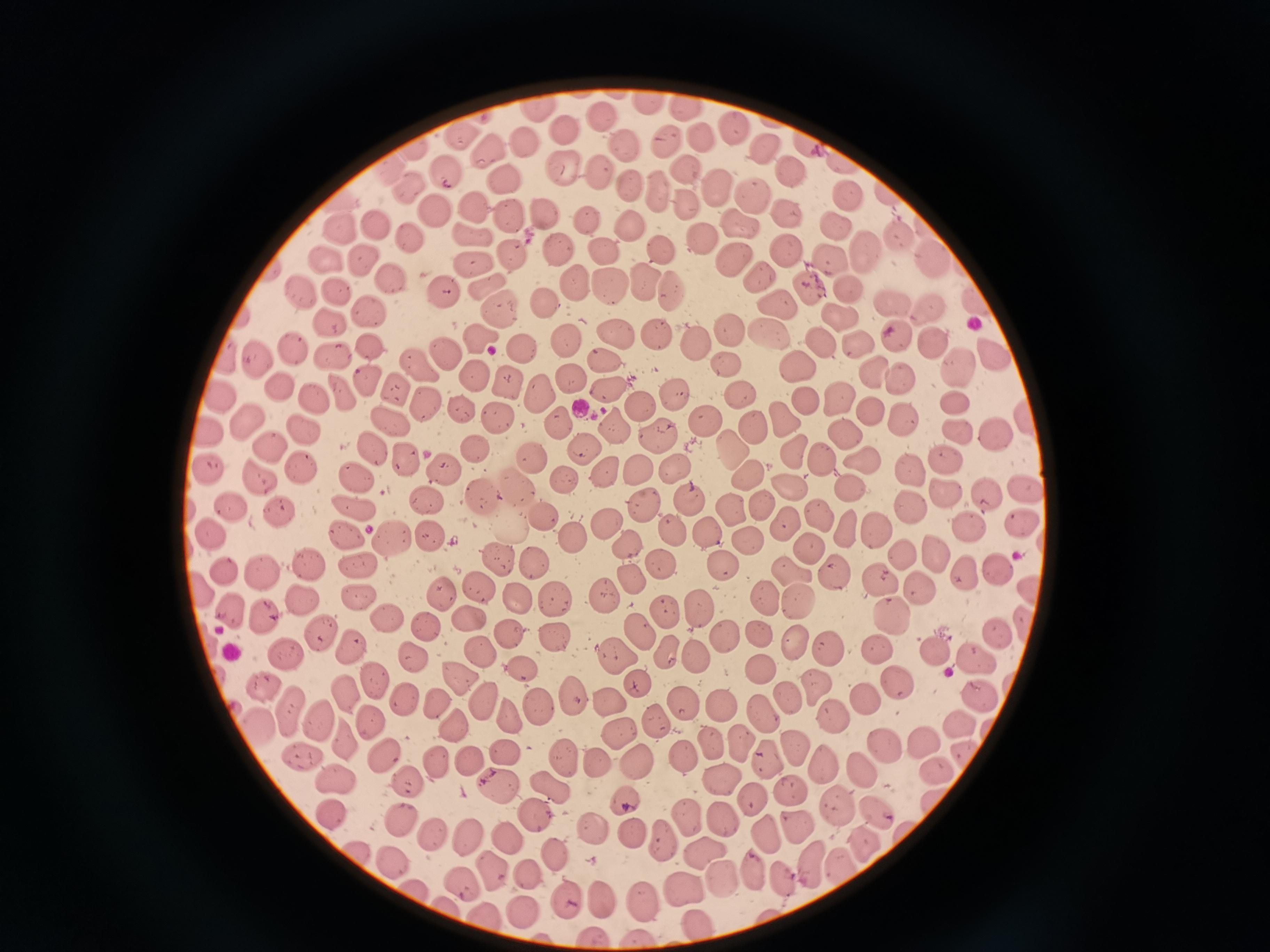
Approximate object centers, in pixels from the top-left corner.
Summary:
  - Cell locations: (x=648, y=104), (x=687, y=108), (x=541, y=109), (x=601, y=117), (x=735, y=128), (x=566, y=134), (x=465, y=137), (x=528, y=141), (x=665, y=141), (x=703, y=142), (x=811, y=144), (x=764, y=146), (x=414, y=148), (x=625, y=148), (x=490, y=154), (x=849, y=159), (x=391, y=170), (x=563, y=171), (x=597, y=171), (x=686, y=171), (x=450, y=172), (x=792, y=172), (x=504, y=181), (x=632, y=185), (x=716, y=186), (x=655, y=188), (x=409, y=193), (x=851, y=197), (x=344, y=198), (x=752, y=198), (x=685, y=202), (x=475, y=208), (x=544, y=211), (x=432, y=213), (x=788, y=215), (x=513, y=217), (x=584, y=219), (x=738, y=224), (x=629, y=226), (x=841, y=226), (x=378, y=227), (x=347, y=229), (x=467, y=232), (x=898, y=234), (x=409, y=237), (x=703, y=238), (x=663, y=248), (x=785, y=248), (x=512, y=249), (x=559, y=251), (x=605, y=252), (x=870, y=255), (x=731, y=256), (x=328, y=258), (x=472, y=261), (x=833, y=261), (x=364, y=262), (x=935, y=262), (x=270, y=267), (x=760, y=275), (x=644, y=278), (x=392, y=280), (x=574, y=285), (x=485, y=287), (x=605, y=287), (x=808, y=288), (x=444, y=290), (x=850, y=290), (x=667, y=291), (x=338, y=292), (x=305, y=293), (x=776, y=299), (x=982, y=302), (x=544, y=303), (x=892, y=303), (x=502, y=307), (x=931, y=308), (x=370, y=314), (x=839, y=316), (x=332, y=321), (x=731, y=329), (x=654, y=332), (x=616, y=333), (x=769, y=333), (x=897, y=333), (x=480, y=338), (x=565, y=339), (x=934, y=343), (x=519, y=344), (x=822, y=344), (x=859, y=344), (x=697, y=345), (x=368, y=346), (x=295, y=350), (x=446, y=354), (x=605, y=355), (x=998, y=355), (x=225, y=356), (x=332, y=357), (x=257, y=360), (x=726, y=363), (x=794, y=363), (x=420, y=365), (x=961, y=365), (x=874, y=374), (x=476, y=375), (x=571, y=377), (x=368, y=379), (x=903, y=380), (x=506, y=382), (x=279, y=385), (x=400, y=388), (x=537, y=392), (x=606, y=392), (x=340, y=394), (x=678, y=394), (x=740, y=394), (x=220, y=396), (x=310, y=397), (x=429, y=400), (x=843, y=400), (x=806, y=401), (x=954, y=401), (x=463, y=408), (x=644, y=409), (x=871, y=415), (x=905, y=416), (x=499, y=417), (x=784, y=418), (x=247, y=419), (x=1029, y=419), (x=557, y=420), (x=705, y=420), (x=394, y=421), (x=613, y=428), (x=754, y=428), (x=959, y=428), (x=309, y=429), (x=659, y=432), (x=208, y=434), (x=998, y=435), (x=850, y=436), (x=271, y=446), (x=584, y=448), (x=736, y=448), (x=373, y=449), (x=474, y=451), (x=797, y=455), (x=824, y=455), (x=406, y=458), (x=864, y=460), (x=532, y=461), (x=673, y=465), (x=949, y=465), (x=308, y=468), (x=442, y=468), (x=638, y=468), (x=909, y=469), (x=748, y=471), (x=212, y=472), (x=606, y=472), (x=358, y=476), (x=261, y=477), (x=566, y=479), (x=513, y=486), (x=792, y=488), (x=1024, y=488), (x=848, y=490), (x=948, y=490), (x=988, y=492), (x=480, y=493), (x=690, y=500), (x=762, y=501), (x=430, y=502), (x=643, y=503), (x=360, y=505), (x=236, y=507), (x=913, y=507), (x=732, y=508), (x=281, y=512), (x=816, y=513), (x=544, y=518), (x=1021, y=518), (x=607, y=523), (x=785, y=524), (x=848, y=524), (x=970, y=526), (x=509, y=527), (x=877, y=529), (x=676, y=530), (x=211, y=533), (x=347, y=533), (x=708, y=533), (x=576, y=535), (x=430, y=538), (x=391, y=539), (x=747, y=541), (x=630, y=546), (x=811, y=546), (x=939, y=551), (x=906, y=554), (x=501, y=559), (x=309, y=561), (x=359, y=561), (x=536, y=562), (x=665, y=564), (x=725, y=564), (x=999, y=567), (x=227, y=571), (x=792, y=572), (x=262, y=573), (x=837, y=575), (x=631, y=576), (x=970, y=576), (x=886, y=579), (x=479, y=588), (x=443, y=590), (x=920, y=590), (x=203, y=594), (x=609, y=595), (x=357, y=596), (x=517, y=597), (x=768, y=598), (x=303, y=600), (x=557, y=604), (x=799, y=604), (x=232, y=608), (x=697, y=609), (x=667, y=612), (x=389, y=616), (x=466, y=616), (x=892, y=616), (x=265, y=620), (x=426, y=629), (x=506, y=633), (x=640, y=633), (x=324, y=634), (x=759, y=634), (x=999, y=635), (x=722, y=637), (x=553, y=638), (x=793, y=641), (x=350, y=645), (x=665, y=648), (x=884, y=648), (x=826, y=649), (x=479, y=652), (x=938, y=654), (x=286, y=655), (x=618, y=655), (x=978, y=655), (x=695, y=656), (x=413, y=657), (x=760, y=666), (x=522, y=668), (x=456, y=676), (x=370, y=677), (x=897, y=677), (x=263, y=683), (x=643, y=683), (x=810, y=688), (x=981, y=691), (x=346, y=693), (x=572, y=695), (x=783, y=696), (x=403, y=697), (x=872, y=700), (x=481, y=701), (x=613, y=702), (x=434, y=704), (x=719, y=704), (x=685, y=705), (x=537, y=707), (x=288, y=709), (x=756, y=709), (x=505, y=713), (x=836, y=716), (x=320, y=718), (x=956, y=719), (x=659, y=720), (x=259, y=723), (x=370, y=723), (x=454, y=726), (x=614, y=729), (x=339, y=733), (x=919, y=737), (x=883, y=740), (x=737, y=743), (x=792, y=746), (x=508, y=752), (x=969, y=752), (x=302, y=753), (x=379, y=753), (x=685, y=756), (x=766, y=756), (x=565, y=758), (x=467, y=760), (x=631, y=760), (x=437, y=761), (x=821, y=761), (x=594, y=765), (x=861, y=766), (x=938, y=769), (x=719, y=778), (x=406, y=779), (x=497, y=781), (x=338, y=782), (x=548, y=785), (x=790, y=789), (x=753, y=801), (x=836, y=803), (x=626, y=806), (x=877, y=811), (x=535, y=813), (x=334, y=817), (x=687, y=817), (x=724, y=820), (x=400, y=824), (x=595, y=825), (x=801, y=827), (x=763, y=832), (x=431, y=834), (x=631, y=837), (x=470, y=838), (x=508, y=839), (x=664, y=843), (x=864, y=845), (x=703, y=854), (x=557, y=857), (x=391, y=858), (x=810, y=861), (x=838, y=865), (x=492, y=867), (x=753, y=869), (x=721, y=875), (x=531, y=877), (x=464, y=880), (x=783, y=880), (x=685, y=886), (x=420, y=890), (x=647, y=899), (x=569, y=900), (x=602, y=901), (x=524, y=910), (x=483, y=916), (x=698, y=921)
  - Preparation: thin blood smear
  - Image size: 1270×952 pixels
  - Stain: Giemsa
  - Field of view: single
  - Capture: smartphone through the microscope eyepiece